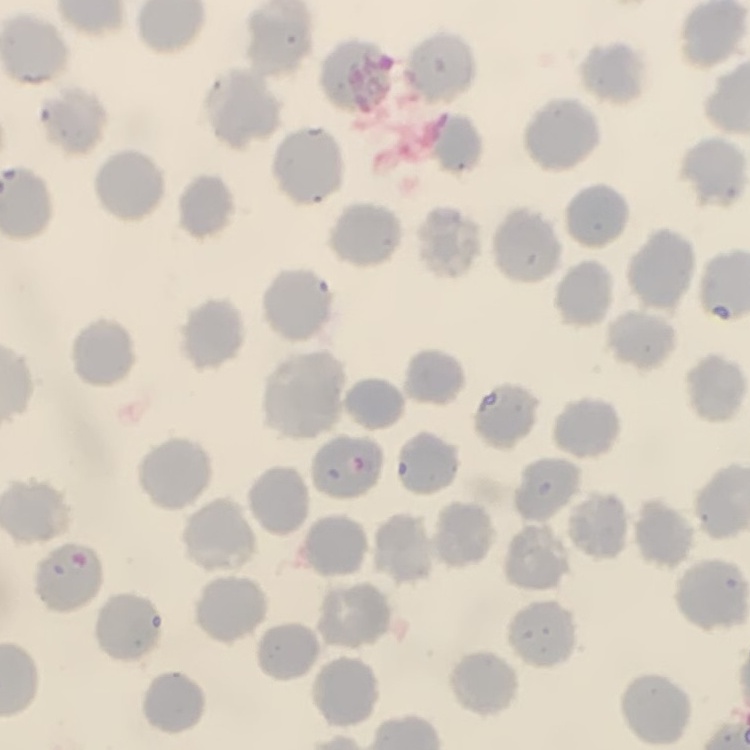
erythrocyte_morphology: no rouleaux formation
preparation: thin blood film
image_type: one tile cut from a larger photomicrograph
stain: Field's or Giemsa